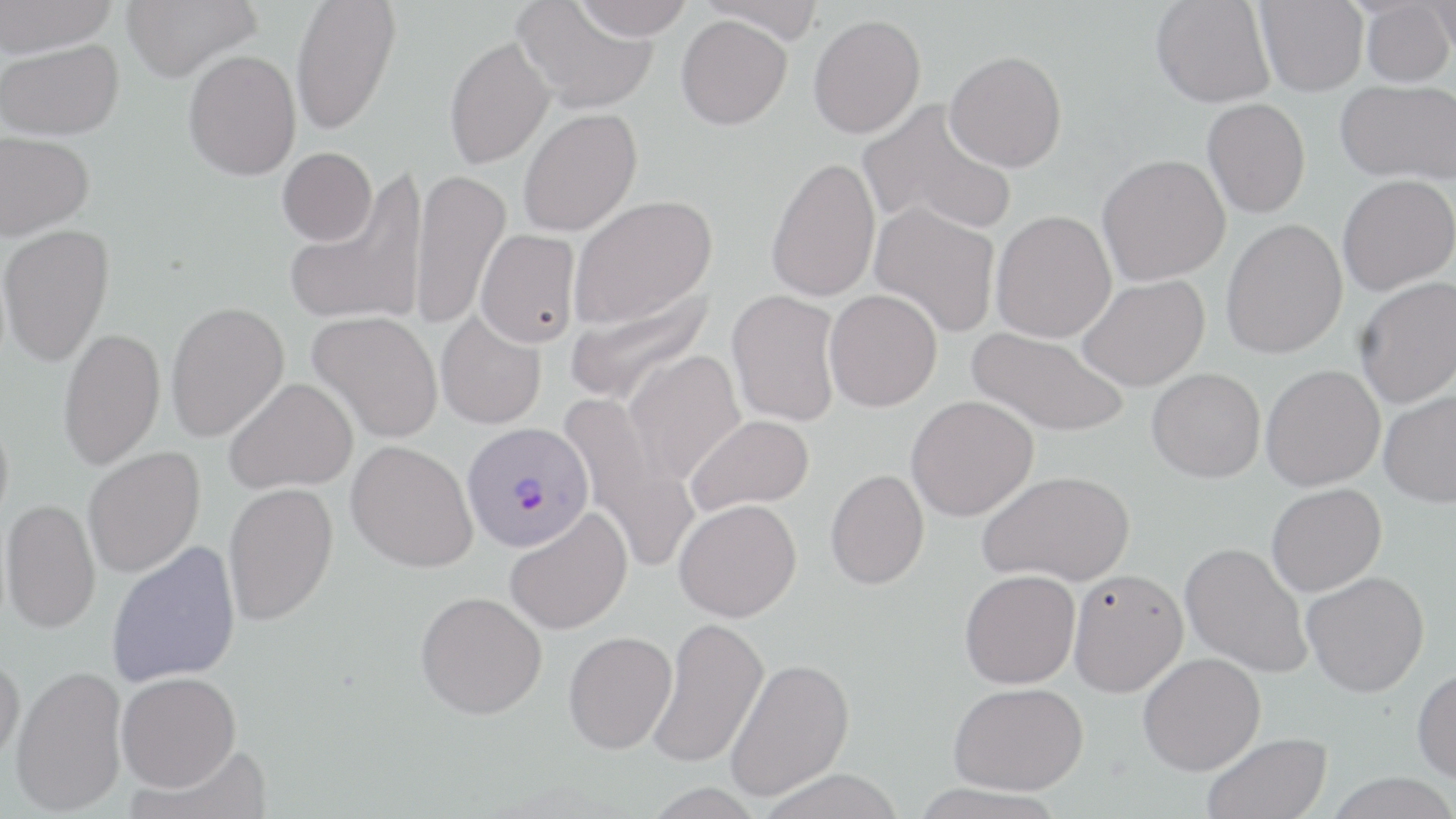
slide_level_diagnosis: Plasmodium vivax
image_size: 1456×819 pixels
preparation: thin blood film
modality: light microscopy
field_of_view: single
stain: May-Grünwald-Giemsa
plasmodium_vivax_infected_red_blood_cell_locations: 'approximate bounding boxes as (x1,y1)-(x2,y2) corner pairs in pixels: (462,422)-(594,552)'
uninfected_red_blood_cell_locations: 'approximate bounding boxes as (x1,y1)-(x2,y2) corner pairs in pixels: (1,0)-(119,56), (121,0)-(261,82), (291,0)-(401,136), (571,0)-(696,39), (698,0)-(826,44), (1255,0)-(1368,96), (1427,0)-(1456,60), (514,1)-(658,114), (1151,1)-(1275,107), (1361,1)-(1454,86), (808,14)-(925,139), (676,15)-(792,130), (444,35)-(555,170), (1,38)-(124,140), (183,50)-(301,180), (945,50)-(1067,171), (1336,79)-(1456,185), (856,98)-(1018,236), (1202,98)-(1310,217), (518,108)-(642,237), (0,131)-(94,240), (277,147)-(377,246), (1097,154)-(1230,285), (766,156)-(881,303), (410,170)-(510,330), (286,172)-(428,328), (1337,174)-(1456,295), (568,195)-(717,329), (870,201)-(1001,338), (991,210)-(1117,343), (1221,218)-(1348,359), (0,224)-(115,367), (476,229)-(581,348), (1077,275)-(1209,391), (1355,276)-(1456,408), (565,285)-(714,407), (824,289)-(942,412), (727,290)-(842,427), (165,301)-(290,443), (307,311)-(444,443), (436,311)-(546,430), (58,327)-(165,471), (968,327)-(1130,438), (623,350)-(746,485), (1261,364)-(1385,491), (1147,368)-(1266,482), (225,377)-(358,494), (1379,391)-(1456,507), (561,395)-(698,574), (906,395)-(1039,521), (0,405)-(13,535), (686,414)-(815,515), (346,440)-(477,572), (83,446)-(206,578), (825,469)-(930,589), (979,470)-(1135,586), (223,482)-(339,626), (1266,483)-(1386,596), (1,498)-(101,634), (674,498)-(802,622), (504,507)-(633,635), (107,540)-(241,687), (1180,542)-(1312,678), (1068,568)-(1189,697), (960,569)-(1080,688), (1302,571)-(1429,697), (416,590)-(547,719), (649,617)-(769,769), (564,630)-(677,754), (1138,651)-(1266,775), (0,652)-(25,765), (726,657)-(855,801), (11,664)-(128,815), (1412,666)-(1456,784), (116,671)-(241,791), (948,682)-(1087,795), (1203,732)-(1331,819), (127,745)-(270,819), (757,767)-(906,818), (1325,772)-(1456,819)'
magnification: 1000x